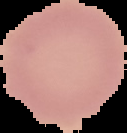
Summary:
  - Image type: cell region segmented out of the field of view; surrounding area masked to black
  - Result: no malaria parasites detected
  - Preparation: thin blood film
  - Image size: 127×133 pixels